Mark where platelets are.
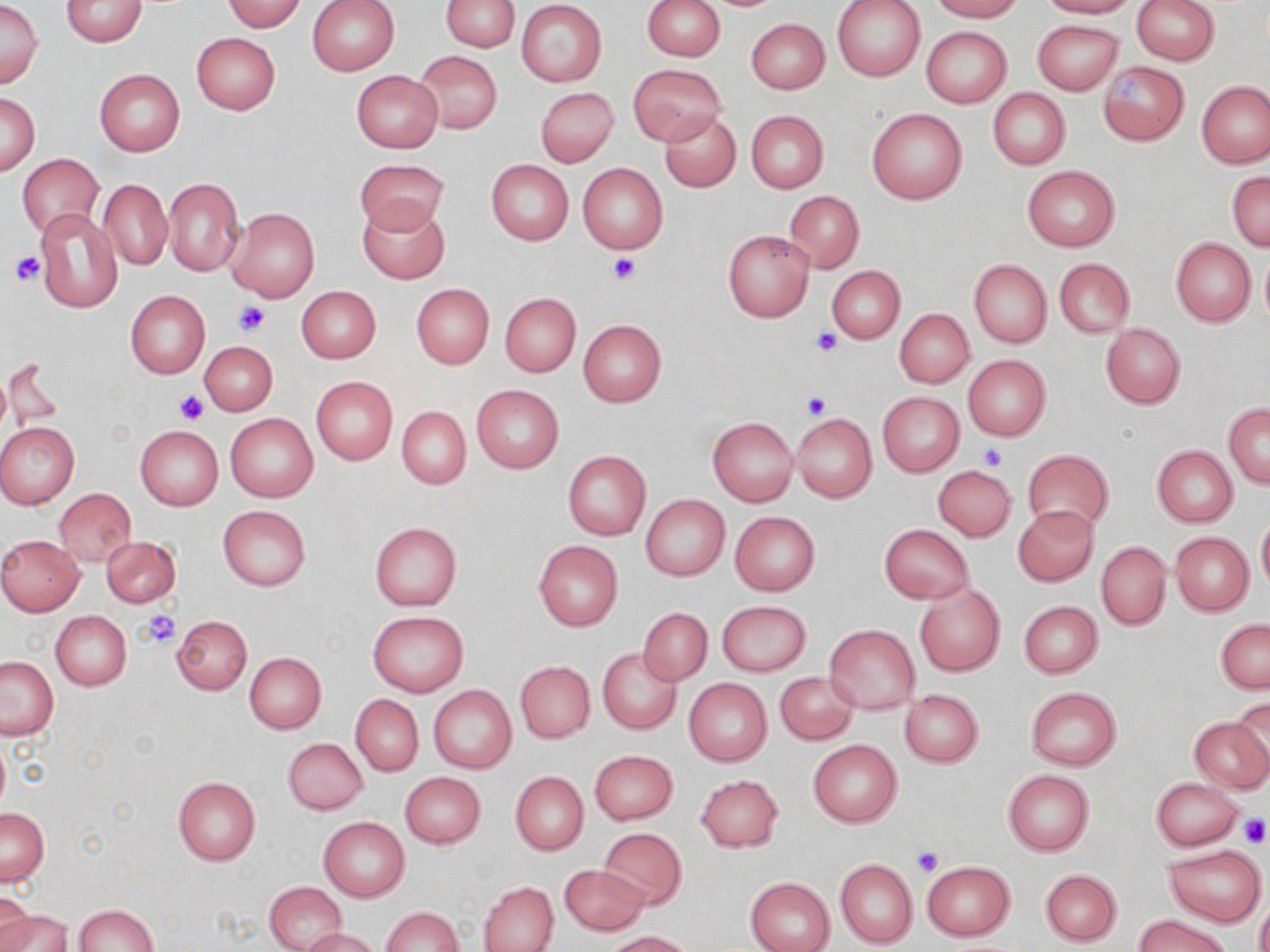
Approximate bounding boxes as [x1, y1, x2, y2] in pixels.
Platelets: [11, 251, 44, 284], [608, 252, 640, 285], [233, 299, 270, 336], [808, 327, 841, 357], [174, 391, 207, 425], [802, 393, 830, 421], [981, 444, 1007, 469], [138, 610, 181, 648], [1237, 813, 1268, 847], [911, 846, 944, 875].

Uninfected red blood cell locations: [61, 0, 147, 47], [308, 0, 398, 75], [441, 0, 518, 50], [643, 0, 725, 61], [832, 0, 926, 81], [928, 0, 1025, 21], [1036, 0, 1137, 18], [1132, 0, 1218, 65], [222, 1, 308, 32], [516, 1, 607, 87], [0, 2, 43, 87], [746, 18, 830, 94], [1032, 19, 1123, 95], [921, 26, 1011, 106], [191, 33, 280, 115], [413, 50, 502, 134], [1098, 60, 1189, 146], [629, 63, 724, 145], [94, 68, 185, 156], [351, 70, 444, 153], [1197, 80, 1270, 168], [536, 87, 617, 166], [988, 88, 1070, 169], [2, 93, 39, 176], [867, 107, 967, 204], [746, 110, 828, 192], [660, 111, 740, 192], [18, 152, 105, 238], [355, 156, 448, 235], [486, 159, 573, 245], [577, 163, 667, 255], [1022, 167, 1120, 252], [1228, 171, 1269, 251], [163, 177, 244, 276], [97, 178, 172, 270], [784, 191, 864, 273], [358, 201, 449, 283], [227, 206, 320, 302], [34, 209, 122, 313], [723, 230, 813, 321], [1171, 239, 1256, 326], [1259, 247, 1270, 331], [1053, 258, 1135, 338], [969, 260, 1051, 349], [828, 266, 905, 343], [410, 283, 494, 368], [296, 285, 381, 363], [125, 290, 210, 379], [500, 293, 580, 378], [895, 309, 974, 387], [578, 319, 666, 407], [1100, 324, 1185, 409], [199, 341, 276, 415], [962, 356, 1051, 442], [2, 357, 63, 434], [310, 375, 397, 465], [472, 385, 564, 473], [877, 391, 964, 477], [1223, 402, 1270, 487], [397, 406, 470, 488], [226, 413, 318, 502], [792, 414, 876, 503], [707, 417, 797, 508], [0, 423, 78, 508], [135, 425, 223, 511], [1152, 446, 1237, 526], [1025, 449, 1113, 531], [563, 451, 650, 540], [933, 467, 1016, 540], [54, 488, 136, 567], [641, 495, 730, 580], [218, 505, 311, 589], [1012, 506, 1097, 585], [730, 512, 820, 595], [1257, 518, 1270, 593], [370, 522, 462, 611], [879, 524, 972, 604], [1170, 532, 1253, 616], [0, 535, 85, 614], [101, 535, 181, 607], [533, 540, 622, 632], [1096, 542, 1171, 631], [913, 583, 1005, 677], [717, 600, 810, 675], [1018, 601, 1102, 678], [637, 607, 712, 686], [51, 610, 131, 690], [367, 612, 468, 697], [172, 615, 251, 695], [1216, 619, 1269, 693], [824, 624, 920, 713], [597, 647, 681, 735], [244, 653, 326, 733], [0, 656, 57, 739], [515, 661, 595, 742], [775, 672, 857, 745], [683, 678, 772, 766], [429, 685, 516, 774], [1025, 686, 1122, 770], [900, 689, 983, 767], [351, 694, 423, 775], [1231, 697, 1270, 781], [1187, 715, 1269, 793], [283, 737, 367, 815], [0, 738, 10, 816], [808, 740, 901, 827], [589, 750, 678, 825], [1003, 770, 1094, 856], [510, 771, 588, 855], [401, 772, 485, 849], [696, 774, 784, 853], [172, 776, 260, 865], [1150, 777, 1244, 850], [0, 808, 50, 886], [319, 816, 409, 901], [598, 828, 688, 909], [1164, 845, 1266, 926], [836, 859, 918, 948], [922, 861, 1015, 940], [560, 864, 648, 935], [1040, 869, 1121, 946], [745, 876, 836, 952], [480, 881, 559, 952], [265, 882, 346, 951], [0, 891, 35, 952], [1255, 896, 1270, 952], [74, 904, 158, 952], [381, 907, 462, 952], [0, 908, 70, 952], [1132, 914, 1235, 952], [298, 928, 381, 951], [602, 931, 692, 951]. Slide-level diagnosis: negative for blood parasites. Image is 1270×952 pixels. May-Grünwald-Giemsa stain. Optical microscopy. Thin blood film. Single field of view. 1000x magnification.